State which parasite is depicted.
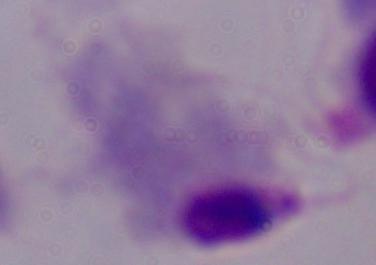
A trichomonad.

magnification = 1000x
modality = micrograph